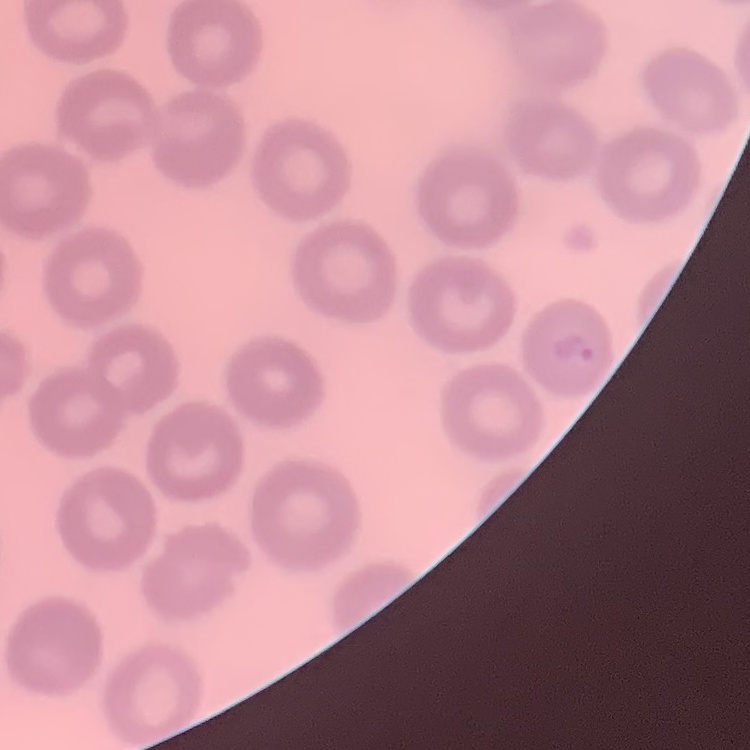
Summary:
  - Red blood cell morphology: no rouleaux formation
  - Image type: one tile cut from a larger photomicrograph
  - Preparation: thin blood film
  - Stain: Field's or Giemsa